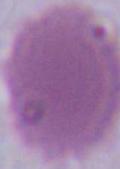
Summary:
  - Identification: erythrocyte
  - Modality: photomicrograph
  - Magnification: 1000x